Assess this cell for malaria.
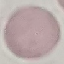
Uninfected.

Summary:
  - Capture: smartphone through the microscope eyepiece
  - Preparation: thin blood film
  - Image type: cell patch, automatically extracted from a larger field of view and resized to 64 × 64 pixels
  - Stain: Giemsa